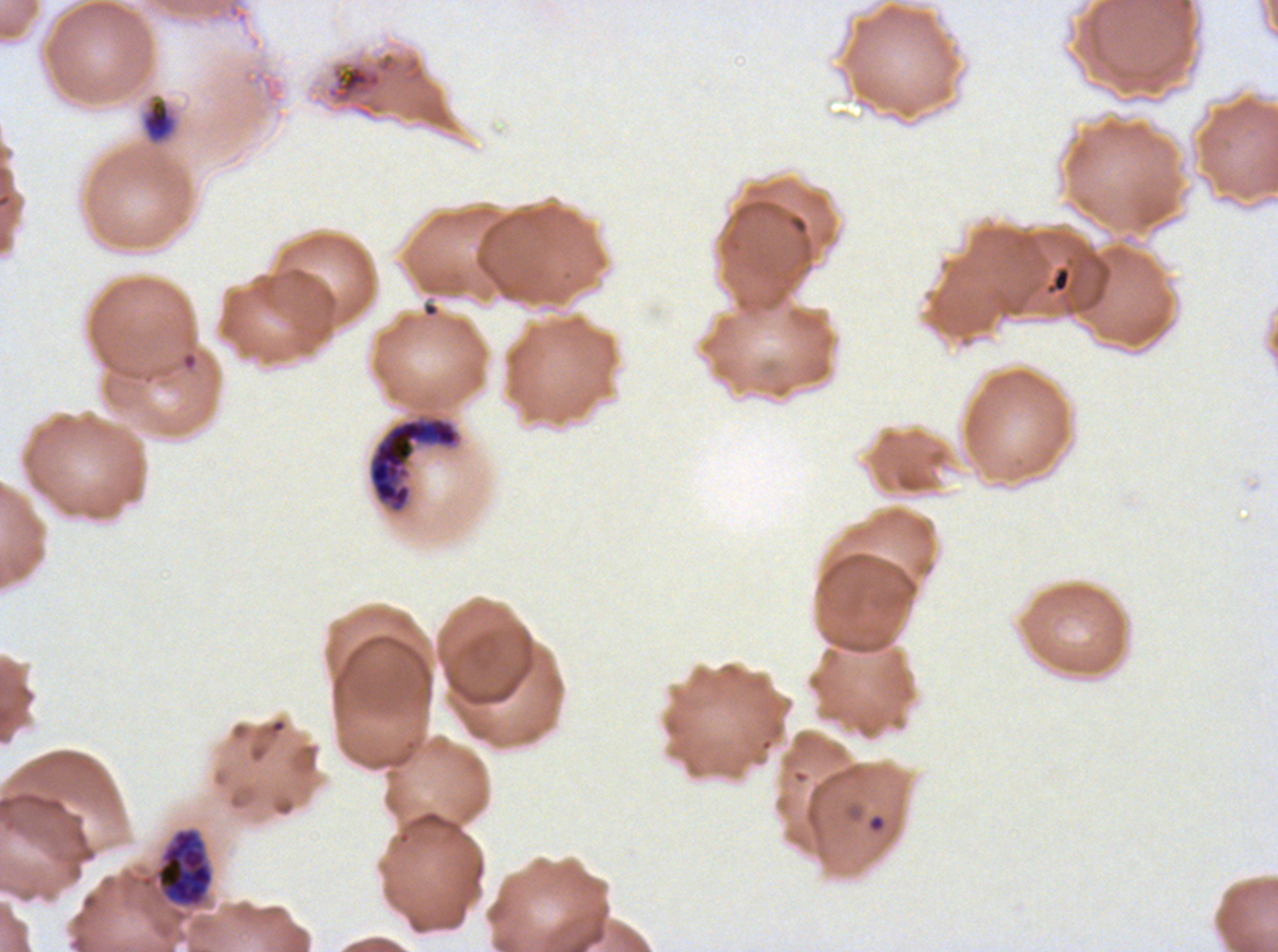

{
  "preparation": "thin blood smear",
  "image_size": "1278×952 pixels",
  "late_schizont_locations": "approximate bounding boxes as (x1, y1, x2, y2) in pixels: (368, 415, 461, 513)",
  "field_of_view": "sub-image separated from a larger composite",
  "early_schizont_locations": "approximate bounding boxes as (x1, y1, x2, y2) in pixels: (154, 827, 215, 908)",
  "specimen": "Plasmodium falciparum cultured ex vivo for 24 to 48 hours, from a patient in The Gambia",
  "ring_locations": "approximate bounding boxes as (x1, y1, x2, y2) in pixels: (866, 813, 886, 833)",
  "life_cycle_stages_observed": "ring, early schizont, late schizont",
  "stain": "Giemsa",
  "debris_locations": "approximate bounding boxes as (x1, y1, x2, y2) in pixels: (325, 51, 426, 119), (141, 97, 178, 145), (1046, 266, 1072, 294)"
}